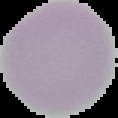

Summary:
  - Malaria status: uninfected
  - Preparation: thin blood smear
  - Image size: 118×118 pixels
  - Image type: cell region segmented out of the field of view; surrounding area masked to black